Evaluate for malaria.
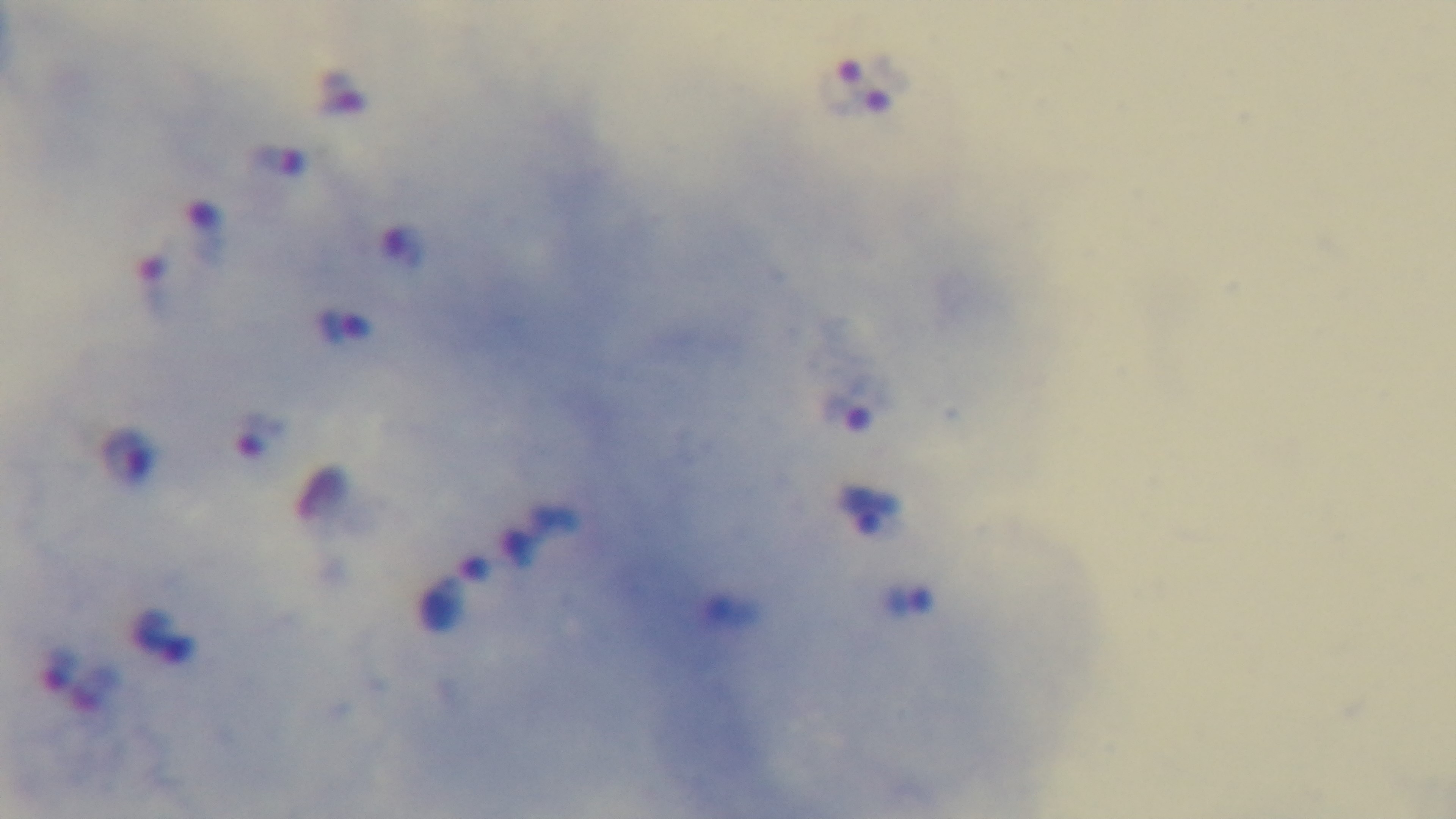
Positive.

Summary:
  - Preparation: thick blood film
  - Stain: Giemsa
  - Capture: mounted 4K digital camera
  - Field of view: single
  - Modality: light microscopy
  - Objective: 100x oil immersion